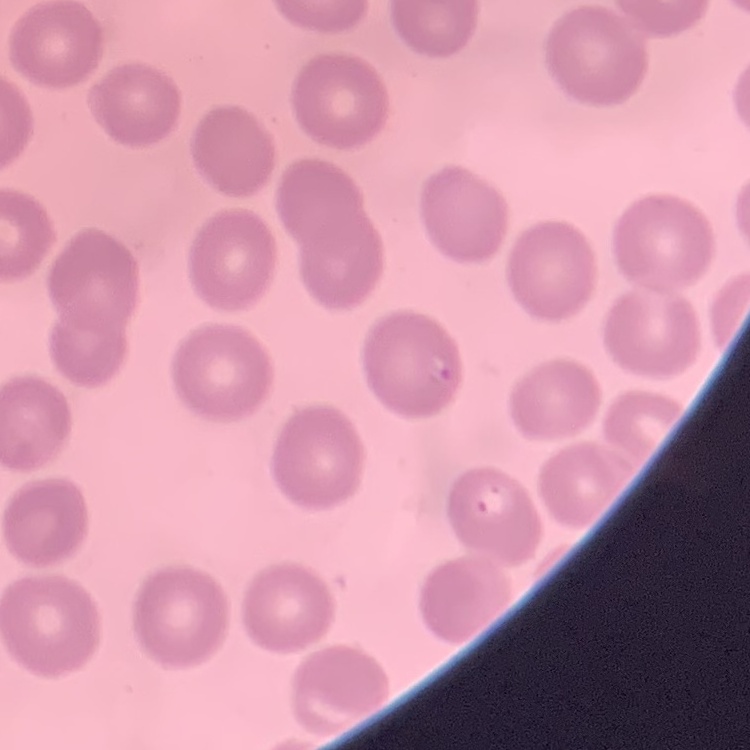
The red blood cells exhibit no rouleaux formation. One tile cut from a larger photomicrograph. Thin peripheral smear. Stained with either Field's or Giemsa.